Report the malaria status of this cell.
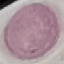
It is uninfected.

image type = automatically extracted cell patch, resized to 64 × 64 pixels
stain = Giemsa
preparation = thin blood smear
capture = smartphone through the microscope eyepiece